Identify the blood parasite species.
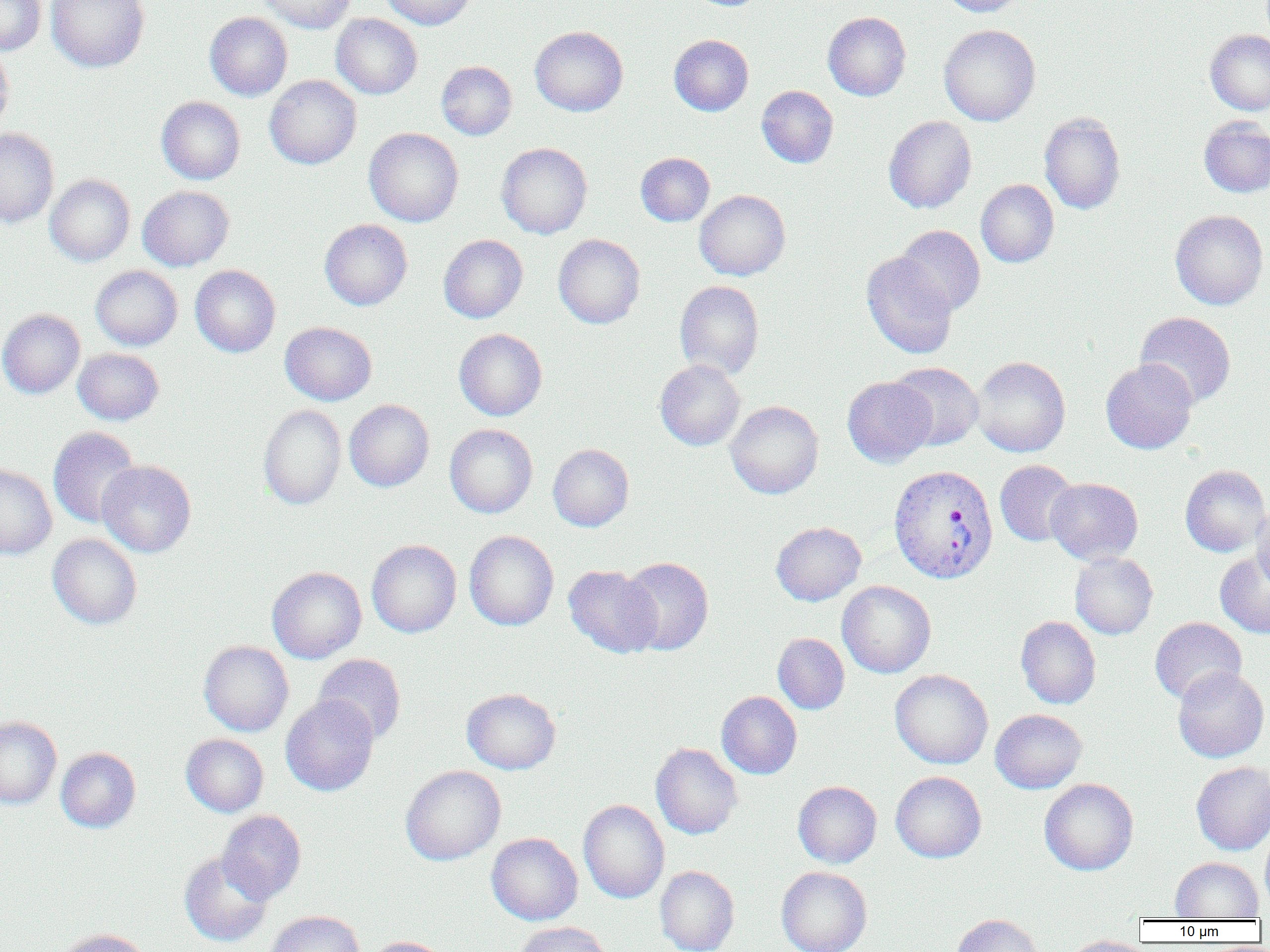
Plasmodium vivax.

Summary:
  - Coordinate format: approximate bounding boxes as named x1/y1/x2/y2 corners in pixels
  - Uninfected red blood cell locations: (x1=0, y1=0, x2=46, y2=54), (x1=46, y1=0, x2=149, y2=72), (x1=256, y1=0, x2=356, y2=33), (x1=380, y1=0, x2=476, y2=29), (x1=940, y1=0, x2=1029, y2=17), (x1=204, y1=11, x2=293, y2=101), (x1=823, y1=11, x2=911, y2=100), (x1=331, y1=13, x2=422, y2=99), (x1=939, y1=24, x2=1040, y2=126), (x1=530, y1=26, x2=628, y2=116), (x1=1205, y1=29, x2=1270, y2=115), (x1=669, y1=34, x2=754, y2=116), (x1=0, y1=43, x2=14, y2=135), (x1=437, y1=61, x2=517, y2=140), (x1=265, y1=75, x2=362, y2=169), (x1=756, y1=86, x2=838, y2=168), (x1=156, y1=96, x2=245, y2=184), (x1=1039, y1=112, x2=1126, y2=214), (x1=884, y1=116, x2=976, y2=213), (x1=1199, y1=116, x2=1270, y2=198), (x1=364, y1=127, x2=463, y2=227), (x1=0, y1=128, x2=59, y2=228), (x1=496, y1=143, x2=592, y2=238), (x1=636, y1=153, x2=715, y2=226), (x1=45, y1=175, x2=135, y2=266), (x1=976, y1=179, x2=1059, y2=268), (x1=138, y1=185, x2=234, y2=271), (x1=694, y1=190, x2=791, y2=280), (x1=1170, y1=209, x2=1268, y2=310), (x1=319, y1=219, x2=412, y2=310), (x1=895, y1=225, x2=985, y2=317), (x1=439, y1=234, x2=528, y2=323), (x1=553, y1=234, x2=645, y2=329), (x1=861, y1=252, x2=957, y2=359), (x1=91, y1=265, x2=183, y2=350), (x1=190, y1=265, x2=280, y2=357), (x1=674, y1=280, x2=764, y2=379), (x1=0, y1=309, x2=85, y2=398), (x1=1135, y1=311, x2=1236, y2=408), (x1=280, y1=322, x2=377, y2=406), (x1=454, y1=328, x2=547, y2=420), (x1=73, y1=348, x2=164, y2=425), (x1=971, y1=356, x2=1071, y2=457), (x1=655, y1=359, x2=745, y2=451), (x1=1101, y1=359, x2=1198, y2=454), (x1=888, y1=362, x2=984, y2=451), (x1=842, y1=377, x2=936, y2=468), (x1=344, y1=399, x2=434, y2=492), (x1=726, y1=400, x2=823, y2=498), (x1=258, y1=404, x2=346, y2=510), (x1=445, y1=424, x2=537, y2=518), (x1=48, y1=426, x2=141, y2=528), (x1=548, y1=444, x2=634, y2=531), (x1=97, y1=460, x2=196, y2=558), (x1=994, y1=460, x2=1079, y2=546), (x1=0, y1=463, x2=57, y2=560), (x1=1180, y1=465, x2=1270, y2=557), (x1=1045, y1=477, x2=1143, y2=565), (x1=1252, y1=504, x2=1270, y2=592), (x1=771, y1=521, x2=866, y2=606), (x1=464, y1=530, x2=559, y2=630), (x1=47, y1=534, x2=142, y2=629), (x1=366, y1=539, x2=461, y2=637), (x1=1215, y1=551, x2=1270, y2=638), (x1=1069, y1=552, x2=1158, y2=639), (x1=618, y1=557, x2=714, y2=655), (x1=563, y1=565, x2=662, y2=658), (x1=267, y1=566, x2=367, y2=663), (x1=837, y1=580, x2=936, y2=678), (x1=1016, y1=616, x2=1102, y2=709), (x1=1149, y1=617, x2=1247, y2=705), (x1=773, y1=633, x2=850, y2=714), (x1=199, y1=640, x2=293, y2=736), (x1=313, y1=654, x2=406, y2=744), (x1=1173, y1=666, x2=1269, y2=762), (x1=889, y1=669, x2=993, y2=769), (x1=462, y1=688, x2=561, y2=774), (x1=716, y1=691, x2=802, y2=779), (x1=280, y1=695, x2=379, y2=796), (x1=990, y1=709, x2=1087, y2=793), (x1=0, y1=716, x2=62, y2=808), (x1=181, y1=733, x2=268, y2=817), (x1=651, y1=743, x2=742, y2=839), (x1=56, y1=747, x2=141, y2=833), (x1=1191, y1=762, x2=1270, y2=855), (x1=401, y1=765, x2=506, y2=865), (x1=891, y1=771, x2=987, y2=863), (x1=1039, y1=778, x2=1138, y2=875), (x1=793, y1=781, x2=882, y2=868), (x1=578, y1=799, x2=669, y2=903), (x1=218, y1=810, x2=306, y2=903), (x1=1260, y1=827, x2=1270, y2=913), (x1=486, y1=832, x2=582, y2=925), (x1=179, y1=851, x2=273, y2=947), (x1=1169, y1=857, x2=1264, y2=920), (x1=655, y1=865, x2=739, y2=952), (x1=776, y1=866, x2=872, y2=952), (x1=265, y1=910, x2=364, y2=952), (x1=951, y1=914, x2=1044, y2=952), (x1=514, y1=921, x2=614, y2=952), (x1=54, y1=928, x2=153, y2=952), (x1=1062, y1=935, x2=1154, y2=952), (x1=364, y1=936, x2=452, y2=952)
  - Plasmodium vivax-infected red blood cell locations: (x1=888, y1=464, x2=999, y2=584)
  - Magnification: 1000x
  - Image size: 1270×952 pixels
  - Field of view: one of a larger specimen
  - Modality: light microscopy
  - Preparation: thin blood film